Give the preparation type.
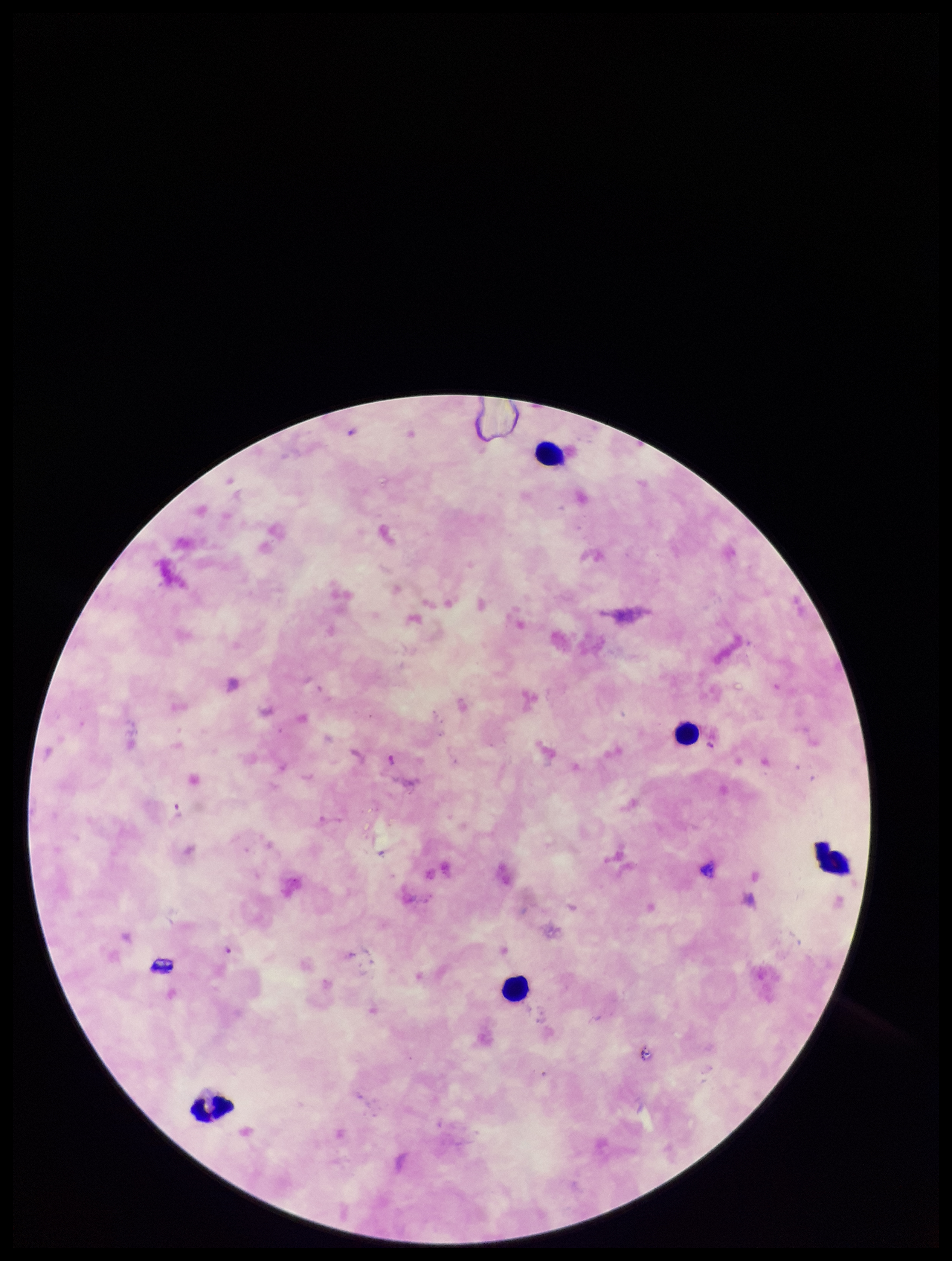

Thick.

Summary:
  - Image size: 952×1261 pixels
  - Plasmodium parasites: none detected
  - Parasite count: 0
  - Patient malaria status: positive
  - Capture: smartphone photograph through the microscope eyepiece
  - Species reported for this patient: Plasmodium falciparum
  - Stain: Giemsa
  - Field of view: one from this slide
  - Leukocyte count: 5